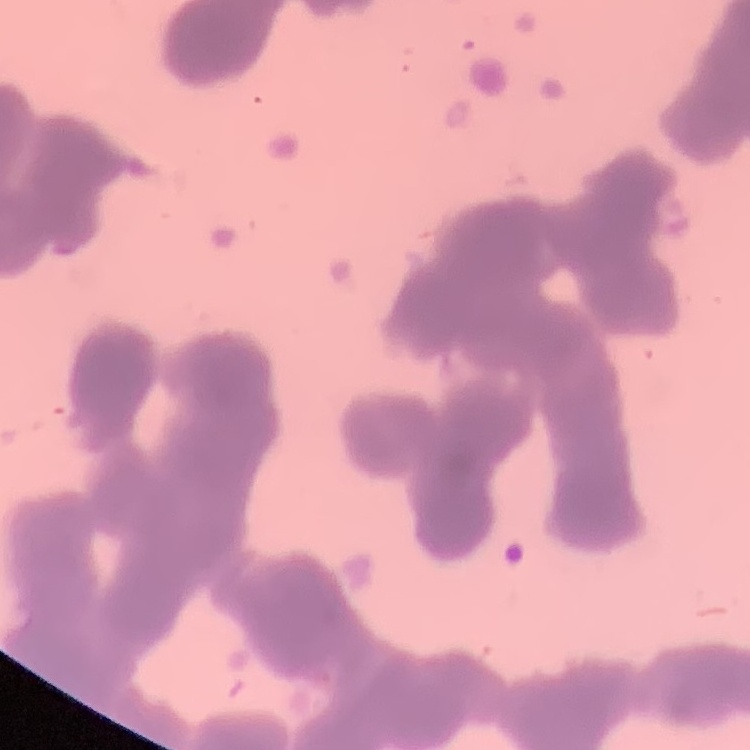 The erythrocytes show rouleaux formation. Stained with either Field's or Giemsa. Thin peripheral smear. Square crop of a larger photomicrograph.